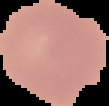

Image is 109×106 pixels. Result: negative for Plasmodium parasites. From a thin blood film. Segmented cell region on a black background.